State which parasite is depicted.
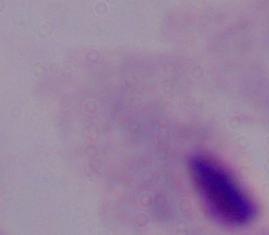

This is a trichomonad.

Summary:
  - Magnification: 1000x
  - Modality: photomicrograph